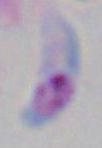 1000x magnification. Toxoplasma gondii is shown. Photomicrograph.